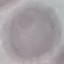
Malaria status: uninfected. Thin blood film. Acquired by smartphone through the microscope eyepiece. Giemsa-stained preparation. Automatically extracted cell patch, resized to 64 × 64 pixels.